State which parasite is depicted.
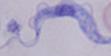
A trypanosome.

1000x magnification. Micrograph.